State the blood parasite species.
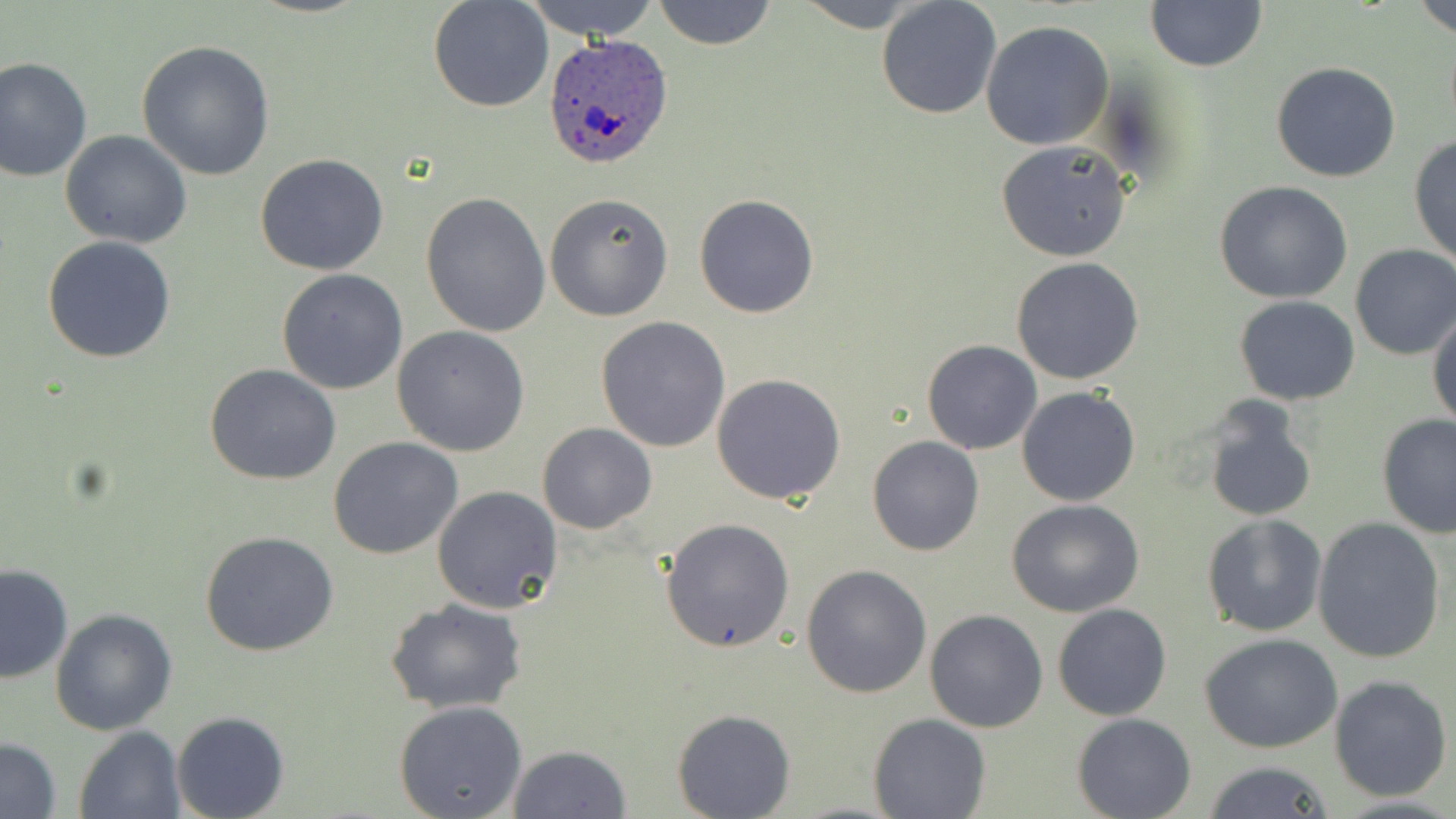

Plasmodium ovale.

Approximate bounding boxes as (x1, y1, x2, y2) in pixels. Plasmodium ovale-infected red blood cell locations: (540, 34, 674, 172). Uninfected red blood cell locations: (521, 0, 665, 41), (652, 0, 778, 51), (793, 0, 932, 29), (875, 0, 1002, 119), (1415, 0, 1456, 39), (428, 1, 554, 113), (1144, 1, 1269, 73), (980, 21, 1115, 151), (136, 39, 276, 181), (0, 56, 93, 181), (1270, 62, 1401, 183), (60, 129, 192, 249), (1410, 136, 1455, 266), (995, 140, 1133, 262), (255, 154, 389, 275), (1213, 181, 1354, 302), (421, 191, 551, 336), (543, 193, 674, 322), (693, 193, 819, 319), (41, 235, 176, 364), (1349, 244, 1456, 360), (1010, 257, 1144, 385), (276, 268, 408, 395), (1234, 296, 1360, 405), (1429, 308, 1456, 431), (596, 316, 731, 452), (391, 326, 530, 457), (921, 339, 1043, 455), (205, 363, 341, 486), (712, 373, 846, 505), (1016, 386, 1141, 507), (1201, 398, 1316, 522), (1377, 412, 1456, 537), (536, 422, 656, 533), (328, 436, 463, 558), (866, 436, 985, 556), (432, 486, 564, 613), (1005, 498, 1145, 617), (1201, 515, 1328, 637), (660, 517, 796, 654), (1312, 517, 1445, 662), (200, 530, 339, 656), (0, 562, 73, 684), (801, 564, 932, 698), (387, 599, 527, 714), (1052, 604, 1172, 721), (50, 607, 178, 737), (925, 608, 1049, 733), (1201, 635, 1344, 754), (1329, 674, 1453, 802), (393, 700, 527, 819), (672, 707, 795, 817), (172, 709, 289, 818), (1072, 712, 1197, 818), (868, 713, 992, 819), (74, 727, 186, 818), (1, 737, 62, 817), (508, 743, 630, 818), (1201, 762, 1338, 818). Image is 1456×819 pixels. Captured at 1000x magnification. One field of a larger specimen. Optical microscopy. Thin blood film. May-Grünwald-Giemsa-stained preparation.